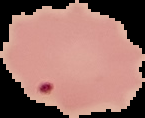
Summary:
  - Image type: segmented cell region with the area outside set to black
  - Malaria status: parasitized
  - Image size: 145×118 pixels
  - Preparation: thin blood film